Name the parasite shown.
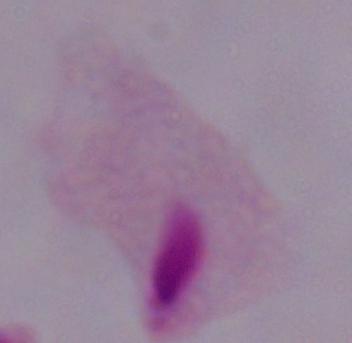

This is a trichomonad.

magnification = 1000x
modality = photomicrograph